Identify the parasite.
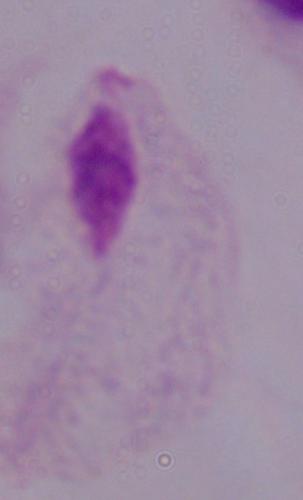
This is a trichomonad.

Summary:
  - Magnification: 1000x
  - Modality: photomicrograph